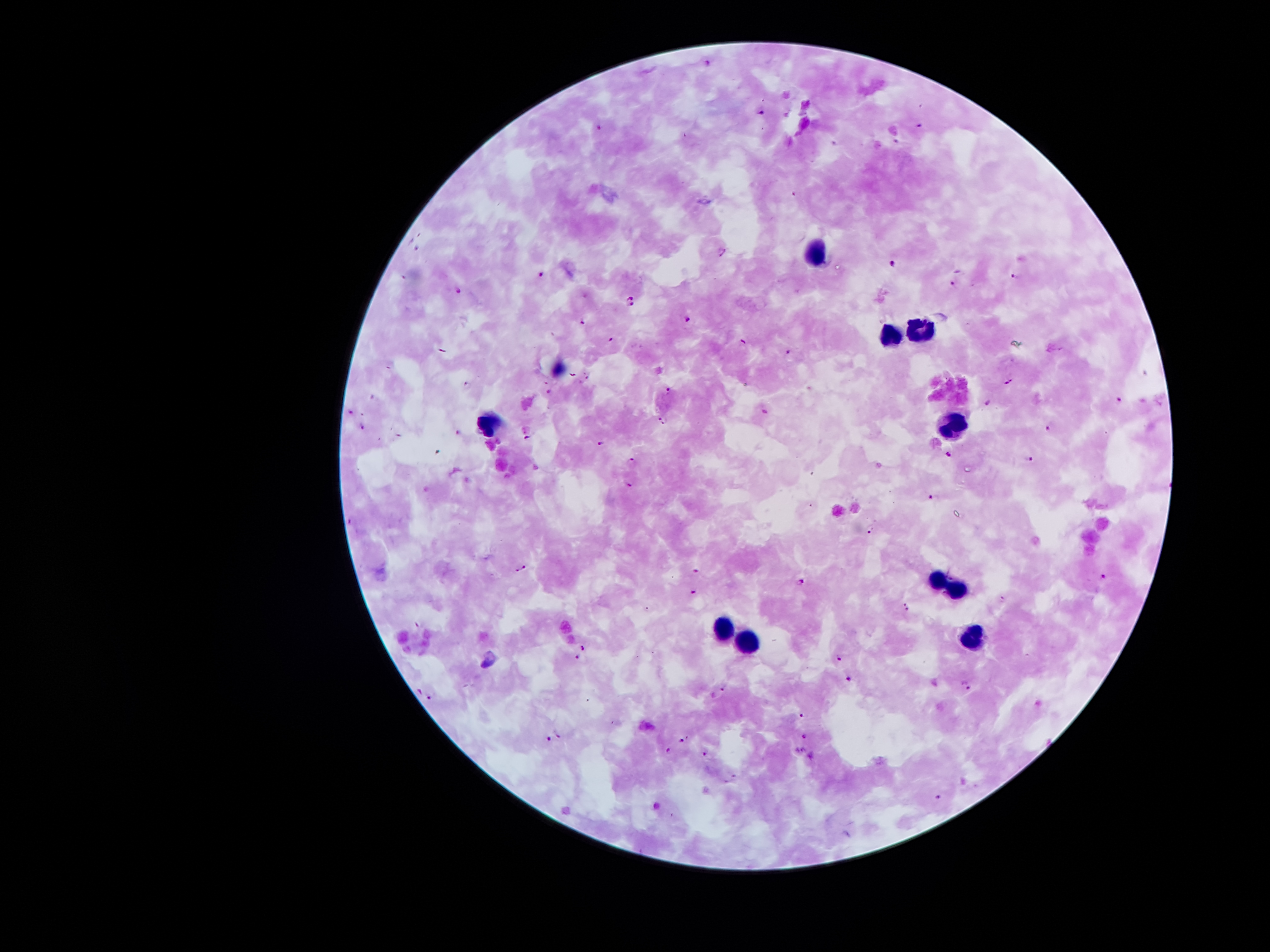
Approximate centers as (x, y) in pixels.
Summary:
  - Leukocyte locations: (815, 250), (919, 327), (889, 332), (490, 419), (955, 423), (937, 578), (959, 589), (723, 628), (974, 637), (746, 643)
  - Plasmodium parasite locations: (707, 64), (761, 115), (600, 124), (918, 125), (723, 252), (891, 264), (540, 274), (1015, 278), (955, 284), (458, 290), (631, 301), (688, 317), (583, 321), (611, 339), (744, 339), (788, 351), (1009, 382), (466, 385), (667, 389), (1118, 402), (988, 403), (351, 411), (663, 421), (1049, 426), (361, 427), (527, 440), (603, 444), (949, 452), (1031, 457), (632, 462), (628, 485), (931, 497), (871, 529), (522, 570), (697, 570), (1105, 576), (801, 581), (692, 592), (1002, 600), (907, 606), (583, 646), (840, 656), (577, 658), (849, 678), (966, 685), (724, 687), (429, 695), (803, 714), (560, 733), (804, 737), (548, 740), (682, 740), (800, 749), (668, 752), (705, 755), (811, 758), (938, 798)
  - Stain: Giemsa
  - Patient malaria status: infected with Plasmodium falciparum
  - Image size: 1270×952 pixels
  - Field of view: single
  - Magnification: 100x
  - Preparation: thick blood film
  - Capture: smartphone through the microscope eyepiece